Locate platelets.
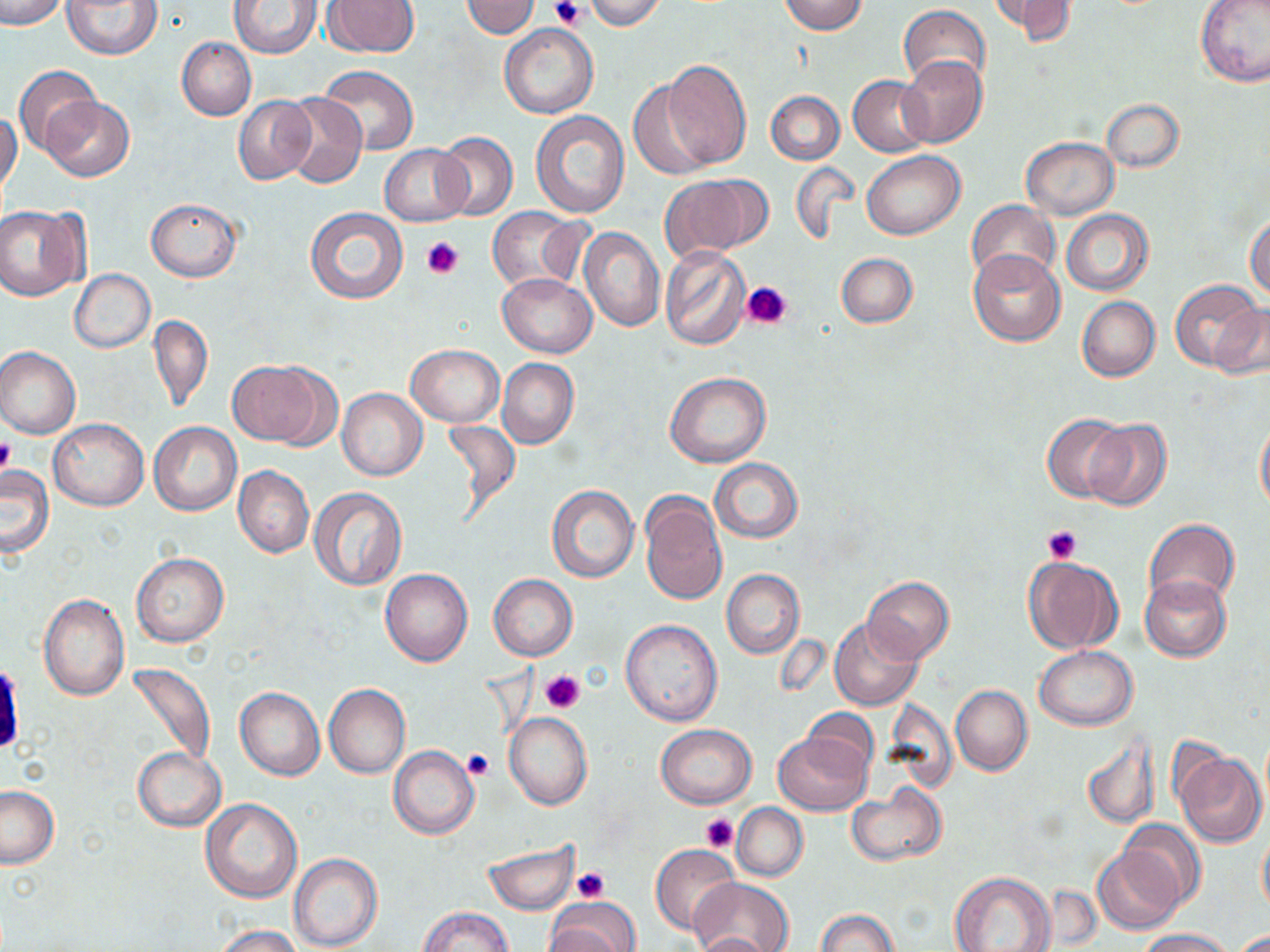
Approximate bounding boxes as named x1/y1/x2/y2 corners in pixels.
Platelets: (x1=551, y1=0, x2=587, y2=28), (x1=420, y1=236, x2=463, y2=280), (x1=741, y1=280, x2=792, y2=331), (x1=0, y1=439, x2=18, y2=475), (x1=1042, y1=525, x2=1082, y2=564), (x1=540, y1=669, x2=586, y2=713), (x1=462, y1=748, x2=494, y2=780), (x1=701, y1=813, x2=737, y2=853), (x1=572, y1=866, x2=609, y2=904).

Summary:
  - Uninfected red blood cell locations: (x1=0, y1=0, x2=67, y2=30), (x1=63, y1=0, x2=163, y2=60), (x1=462, y1=0, x2=540, y2=38), (x1=584, y1=0, x2=665, y2=30), (x1=780, y1=0, x2=867, y2=35), (x1=991, y1=0, x2=1075, y2=42), (x1=1195, y1=0, x2=1270, y2=87), (x1=228, y1=1, x2=320, y2=57), (x1=324, y1=1, x2=420, y2=56), (x1=899, y1=6, x2=992, y2=92), (x1=498, y1=22, x2=597, y2=119), (x1=177, y1=37, x2=257, y2=120), (x1=898, y1=55, x2=988, y2=147), (x1=662, y1=60, x2=751, y2=170), (x1=14, y1=65, x2=102, y2=156), (x1=320, y1=67, x2=418, y2=156), (x1=849, y1=75, x2=933, y2=157), (x1=627, y1=81, x2=716, y2=179), (x1=765, y1=91, x2=843, y2=165), (x1=282, y1=93, x2=367, y2=188), (x1=43, y1=96, x2=135, y2=181), (x1=233, y1=96, x2=316, y2=186), (x1=1101, y1=98, x2=1184, y2=173), (x1=530, y1=111, x2=629, y2=218), (x1=0, y1=112, x2=22, y2=198), (x1=434, y1=132, x2=517, y2=221), (x1=1021, y1=137, x2=1118, y2=219), (x1=380, y1=143, x2=472, y2=227), (x1=863, y1=151, x2=965, y2=240), (x1=790, y1=161, x2=858, y2=243), (x1=659, y1=176, x2=765, y2=262), (x1=146, y1=198, x2=241, y2=281), (x1=966, y1=199, x2=1060, y2=284), (x1=0, y1=206, x2=86, y2=299), (x1=487, y1=207, x2=584, y2=291), (x1=306, y1=208, x2=409, y2=306), (x1=1061, y1=209, x2=1153, y2=295), (x1=1245, y1=213, x2=1270, y2=302), (x1=579, y1=227, x2=665, y2=332), (x1=660, y1=246, x2=752, y2=349), (x1=970, y1=249, x2=1065, y2=346), (x1=835, y1=253, x2=918, y2=327), (x1=69, y1=269, x2=155, y2=354), (x1=497, y1=273, x2=597, y2=357), (x1=1171, y1=278, x2=1262, y2=370), (x1=1077, y1=296, x2=1160, y2=382), (x1=1209, y1=302, x2=1270, y2=380), (x1=148, y1=314, x2=213, y2=412), (x1=406, y1=343, x2=504, y2=427), (x1=0, y1=346, x2=81, y2=440), (x1=497, y1=358, x2=579, y2=449), (x1=227, y1=360, x2=332, y2=446), (x1=664, y1=372, x2=772, y2=468), (x1=337, y1=388, x2=428, y2=481), (x1=1043, y1=413, x2=1128, y2=502), (x1=1255, y1=416, x2=1270, y2=513), (x1=441, y1=417, x2=521, y2=516), (x1=48, y1=418, x2=148, y2=511), (x1=1083, y1=420, x2=1172, y2=511), (x1=149, y1=422, x2=241, y2=516), (x1=710, y1=458, x2=802, y2=542), (x1=233, y1=465, x2=313, y2=559), (x1=0, y1=466, x2=54, y2=556), (x1=546, y1=486, x2=639, y2=583), (x1=309, y1=489, x2=407, y2=591), (x1=639, y1=491, x2=729, y2=606), (x1=1144, y1=518, x2=1240, y2=611), (x1=131, y1=552, x2=229, y2=647), (x1=1023, y1=556, x2=1124, y2=655), (x1=379, y1=568, x2=473, y2=666), (x1=721, y1=569, x2=805, y2=659), (x1=488, y1=574, x2=578, y2=661), (x1=1140, y1=574, x2=1232, y2=662), (x1=862, y1=576, x2=953, y2=664), (x1=39, y1=594, x2=129, y2=700), (x1=620, y1=618, x2=723, y2=726), (x1=830, y1=619, x2=924, y2=711), (x1=1034, y1=646, x2=1138, y2=731), (x1=126, y1=662, x2=216, y2=769), (x1=324, y1=684, x2=410, y2=778), (x1=951, y1=684, x2=1032, y2=776), (x1=234, y1=688, x2=325, y2=781), (x1=804, y1=709, x2=876, y2=773), (x1=504, y1=711, x2=592, y2=810), (x1=656, y1=724, x2=756, y2=808), (x1=773, y1=731, x2=872, y2=816), (x1=1081, y1=735, x2=1158, y2=831), (x1=132, y1=747, x2=225, y2=831), (x1=389, y1=747, x2=480, y2=839), (x1=1173, y1=749, x2=1267, y2=847), (x1=846, y1=782, x2=947, y2=867), (x1=0, y1=786, x2=59, y2=868), (x1=200, y1=799, x2=302, y2=903), (x1=733, y1=803, x2=808, y2=881), (x1=1118, y1=819, x2=1205, y2=907), (x1=1257, y1=824, x2=1270, y2=920), (x1=482, y1=840, x2=581, y2=915), (x1=1093, y1=844, x2=1186, y2=935), (x1=650, y1=845, x2=741, y2=935), (x1=289, y1=852, x2=383, y2=952), (x1=949, y1=871, x2=1056, y2=952), (x1=689, y1=876, x2=792, y2=952), (x1=546, y1=897, x2=640, y2=952), (x1=420, y1=908, x2=513, y2=952), (x1=815, y1=908, x2=899, y2=951), (x1=212, y1=925, x2=303, y2=952), (x1=1134, y1=928, x2=1234, y2=951), (x1=1235, y1=929, x2=1270, y2=950), (x1=693, y1=931, x2=777, y2=951)
  - Slide-level diagnosis: no evidence of blood parasites
  - Image size: 1270×952 pixels
  - Preparation: thin blood film
  - Magnification: 1000x
  - Modality: optical microscopy
  - Field of view: one of a larger specimen
  - Stain: May-Grünwald-Giemsa